Report the malaria status of this cell.
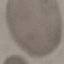

Uninfected.

Giemsa stain. Cell patch, automatically extracted from a larger field of view and resized to 64 × 64 pixels. Photographed with a smartphone camera at the microscope eyepiece. Thin blood smear.